Outline each blood parasite and name the species.
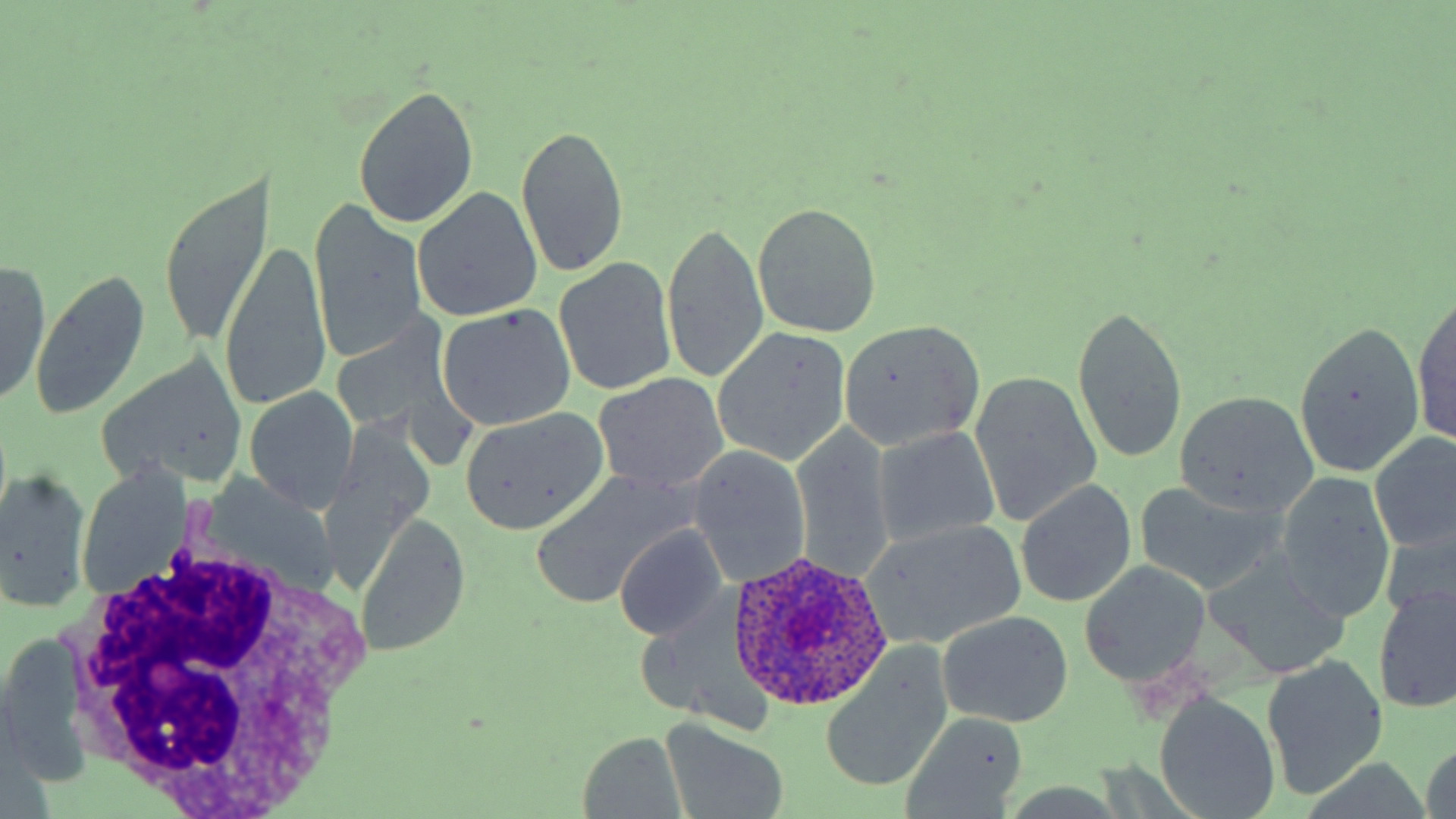

Approximate bounding boxes as (x1,y1)-(x2,y2) corner pairs in pixels.
Plasmodium ovale-infected red blood cells: (725,551)-(896,712).
No Plasmodium falciparum, Plasmodium malariae, Plasmodium vivax, Babesia divergens, or Trypanosoma brucei observed.

slide-level diagnosis = Plasmodium ovale
modality = light microscopy
stain = May-Grünwald-Giemsa
field of view = one of a larger specimen
uninfected red blood cell locations = approximate bounding boxes as (x1,y1)-(x2,y2) corner pairs in pixels: (353,83)-(479,230), (516,126)-(629,276), (158,176)-(271,344), (416,189)-(541,323), (309,200)-(428,369), (752,202)-(881,336), (662,220)-(769,386), (219,240)-(331,416), (556,255)-(678,397), (0,259)-(51,410), (31,270)-(151,419), (1412,292)-(1456,452), (1070,301)-(1187,468), (437,304)-(576,433), (328,312)-(468,452), (838,318)-(988,452), (1289,322)-(1427,479), (711,327)-(851,467), (98,350)-(251,492), (970,369)-(1102,528), (593,372)-(728,497), (245,386)-(357,513), (1173,391)-(1317,519), (456,408)-(609,536), (791,422)-(896,585), (873,426)-(1004,546), (1371,431)-(1455,555), (688,446)-(813,587), (1,469)-(92,614), (530,471)-(694,611), (1275,473)-(1397,625), (1016,478)-(1137,609), (1134,480)-(1283,596), (354,511)-(470,660), (860,518)-(1029,651), (1380,521)-(1455,631), (615,526)-(728,641), (1206,555)-(1352,679), (1081,562)-(1210,688), (1373,583)-(1455,715), (938,612)-(1074,729), (1,631)-(92,789), (819,649)-(952,793), (1262,657)-(1390,800), (1158,697)-(1281,818), (903,712)-(1030,815), (660,718)-(790,819), (578,732)-(689,817)
magnification = 1000x
preparation = thin blood smear
image size = 1456×819 pixels
white blood cell locations = approximate bounding boxes as (x1,y1)-(x2,y2) corner pairs in pixels: (57,534)-(382,811)